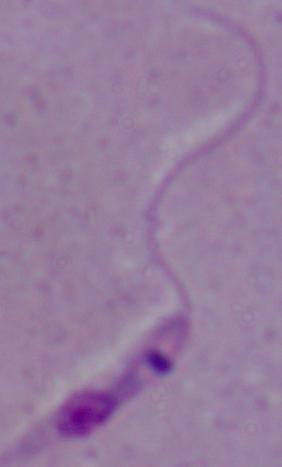

Photomicrograph. Captured at 1000x magnification. A Leishmania parasite is seen.